Outline each blood parasite and name the species.
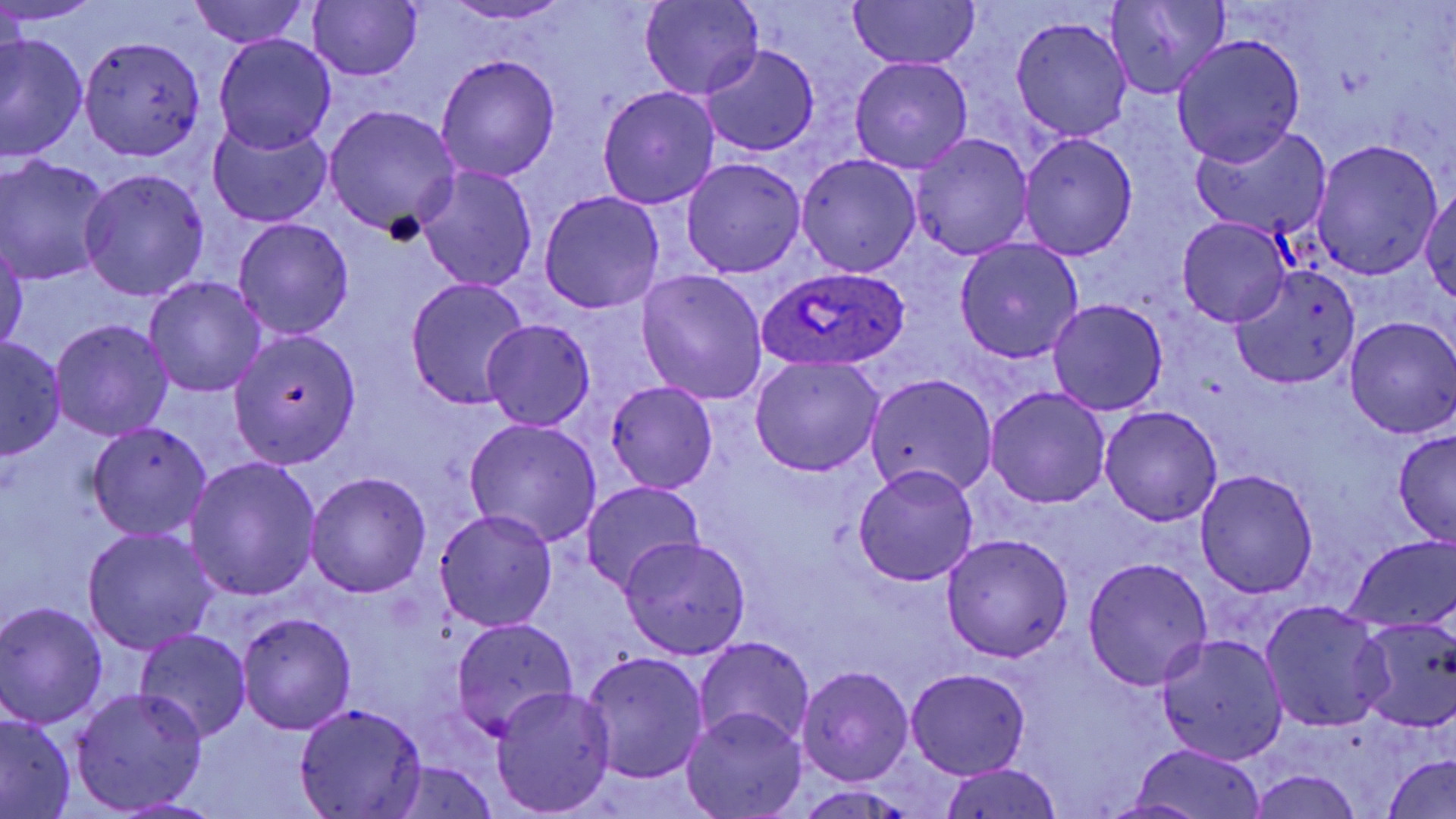
Approximate bounding boxes as [x1, y1, x2, y2] in pixels.
Plasmodium ovale-infected red blood cells: [756, 265, 910, 372].
No Plasmodium falciparum, Plasmodium malariae, Plasmodium vivax, Babesia divergens, or Trypanosoma brucei observed.

slide-level diagnosis = Plasmodium ovale
preparation = thin blood film
field of view = single
modality = light microscopy
uninfected red blood cell locations = approximate bounding boxes as [x1, y1, x2, y2] in pixels: [0, 0, 103, 25], [188, 0, 310, 49], [308, 0, 423, 82], [441, 1, 575, 24], [640, 1, 762, 101], [846, 1, 980, 71], [1105, 1, 1229, 99], [1011, 17, 1133, 141], [1, 33, 87, 163], [214, 33, 337, 155], [1172, 33, 1307, 166], [80, 35, 207, 160], [702, 44, 819, 157], [435, 53, 562, 183], [850, 56, 973, 173], [597, 86, 719, 209], [326, 105, 460, 237], [209, 120, 333, 227], [1193, 124, 1332, 239], [1020, 133, 1137, 260], [910, 134, 1033, 260], [1310, 139, 1443, 276], [796, 153, 921, 277], [0, 156, 114, 284], [681, 157, 806, 277], [415, 167, 538, 292], [78, 168, 210, 301], [1421, 185, 1455, 305], [539, 191, 665, 315], [232, 217, 354, 339], [1177, 217, 1292, 327], [0, 236, 27, 359], [955, 240, 1083, 363], [1234, 261, 1362, 387], [635, 270, 768, 404], [144, 276, 268, 397], [406, 277, 531, 410], [1048, 298, 1168, 416], [1345, 316, 1456, 440], [482, 318, 596, 430], [50, 319, 173, 441], [229, 329, 362, 465], [1, 338, 67, 460], [748, 356, 885, 476], [865, 373, 999, 497], [604, 381, 718, 495], [985, 388, 1111, 508], [1100, 406, 1223, 526], [464, 418, 603, 547], [86, 422, 212, 542], [1392, 428, 1456, 546], [186, 456, 322, 600], [853, 465, 980, 587], [1194, 468, 1319, 598], [306, 472, 431, 597], [580, 479, 705, 596], [434, 508, 558, 632], [84, 530, 219, 652], [941, 533, 1074, 663], [620, 535, 751, 660], [1345, 536, 1455, 634], [1082, 557, 1214, 689], [1260, 600, 1390, 733], [1, 601, 108, 727], [235, 612, 356, 735], [1354, 617, 1456, 732], [449, 618, 576, 741], [133, 628, 251, 743], [1154, 633, 1288, 764], [693, 635, 815, 752], [580, 651, 710, 783], [797, 666, 914, 786], [906, 668, 1030, 779], [490, 686, 615, 816], [70, 687, 207, 812], [295, 703, 427, 818], [683, 708, 806, 819], [0, 714, 77, 817], [1123, 742, 1267, 819], [1383, 753, 1455, 818], [382, 763, 504, 819], [940, 764, 1064, 819], [1246, 769, 1364, 819], [790, 786, 923, 819], [1096, 797, 1216, 817]
stain = May-Grünwald-Giemsa
magnification = 1000x
image size = 1456×819 pixels